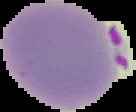
Segmented cell region on a black background. Image is 136×112 pixels. Malaria status: parasitized. From a thin blood film.